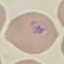

Summary:
  - Malaria status: parasitized
  - Stain: Giemsa
  - Preparation: thin smear
  - Image type: automatically extracted cell patch, resized to 64 × 64 pixels
  - Capture: smartphone camera at the microscope eyepiece